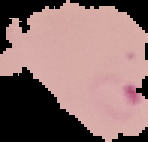
{
  "preparation": "thin blood film",
  "image_type": "cell region segmented out of the field of view; surrounding area masked to black",
  "image_size": "148×142 pixels",
  "malaria_status": "parasitized"
}